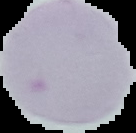 The area outside the segmented cell region is set to black. Malaria status: uninfected. From a thin blood smear. Image is 136×133 pixels.